Assess the morphology of the erythrocytes.
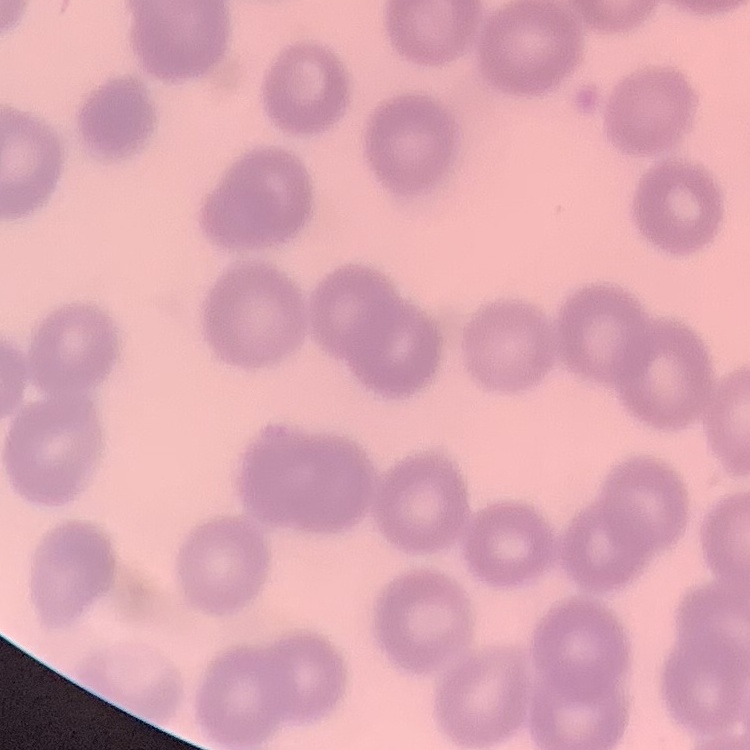

They show no rouleaux formation.

image type = one tile cut from a larger photomicrograph
preparation = thin blood smear
stain = Field's or Giemsa